Assess the morphology of the red blood cells.
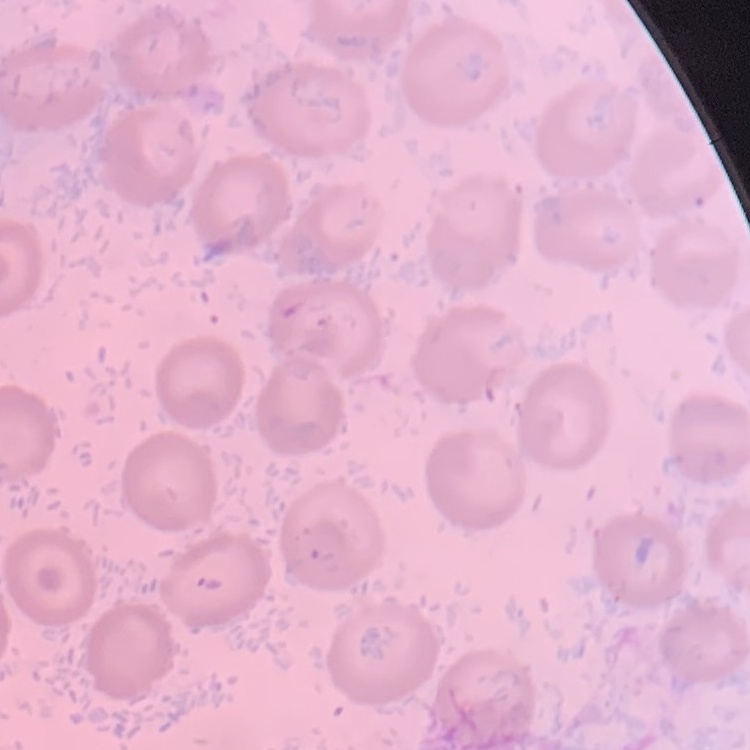
They show no rouleaux formation.

Summary:
  - Stain: Field's or Giemsa
  - Preparation: thin blood film
  - Image type: one tile cut from a larger photomicrograph